Evaluate for Plasmodium parasites.
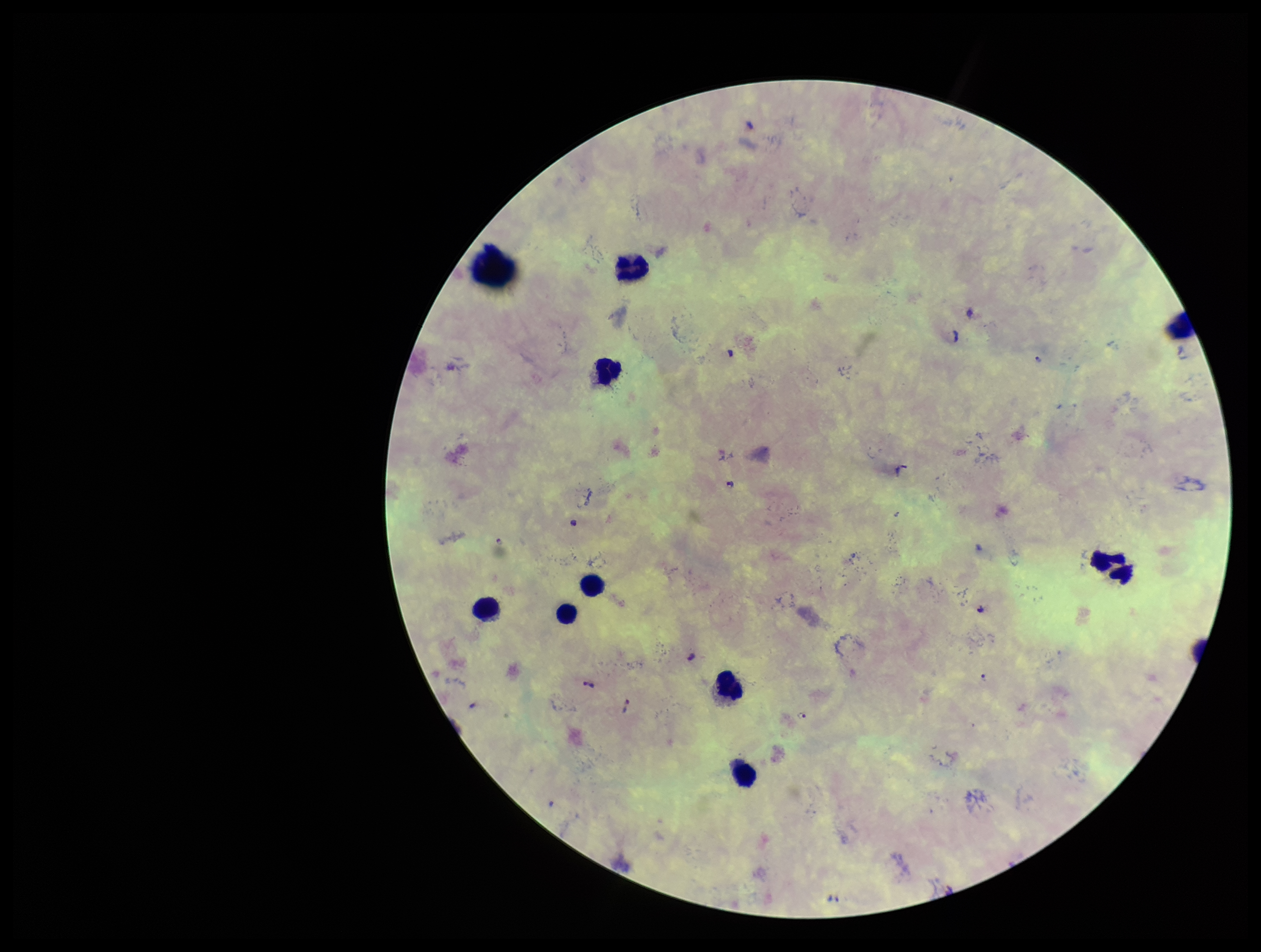

Seen.

Summary:
  - Capture: smartphone photograph through the microscope eyepiece
  - Leukocyte count: 9
  - Field of view: single
  - Image size: 1261×952 pixels
  - Parasite count: 5
  - Stain: Giemsa
  - Patient malaria status: infected
  - Species reported for this patient: Plasmodium falciparum
  - Preparation: thick smear